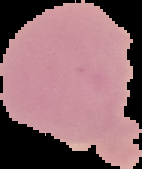

Summary:
  - Result: negative for malaria parasites
  - Image type: segmented cell region on a black background
  - Image size: 142×169 pixels
  - Preparation: thin blood smear